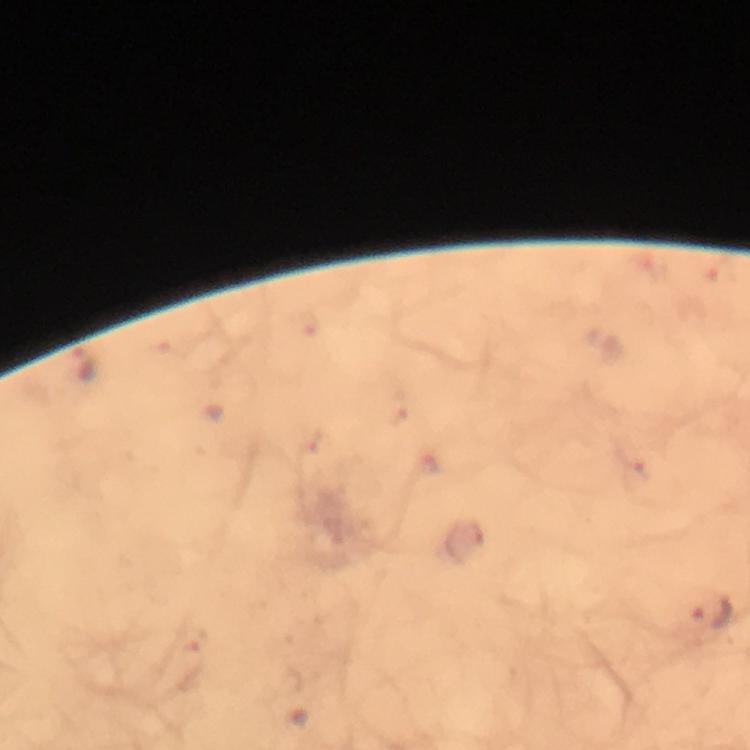
malaria parasite locations = approximate centers as {x, y} in pixels: {86, 365}, {309, 440}, {712, 614}, {191, 638}
capture = smartphone mounted on the microscope
context = from a malaria diagnostic workup
immersion oil = used
magnification = 100x
cropped from = one field of view
stain = Giemsa
preparation = thick blood smear
image size = 750×750 pixels